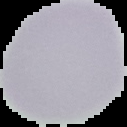
image type = segmented cell region on a black background
preparation = thin blood smear
image size = 127×127 pixels
result = negative for malaria parasites